Outline each blood parasite and name the species.
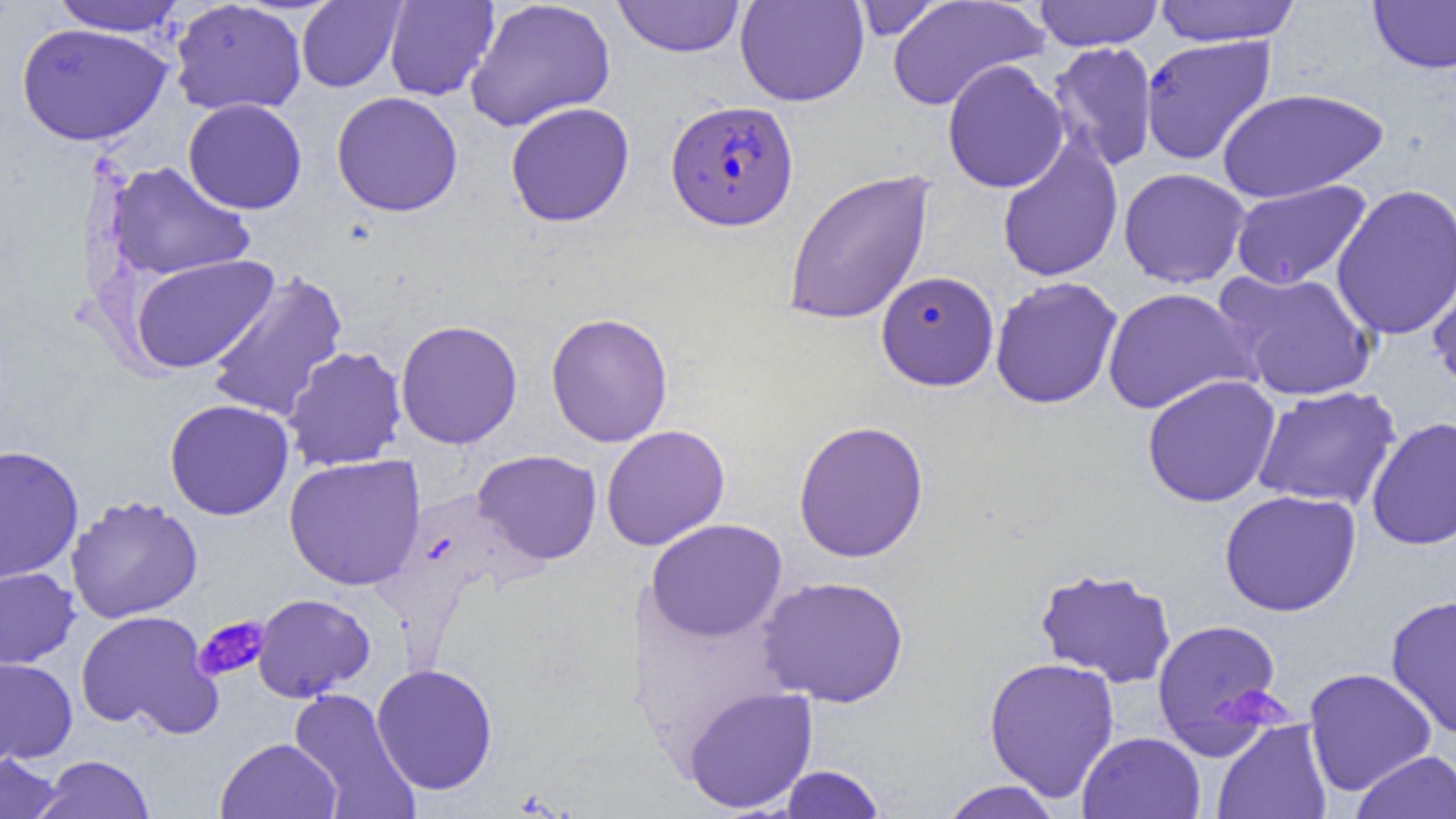

Approximate bounding boxes as named x1/y1/x2/y2 corners in pixels.
Plasmodium falciparum-infected red blood cells (subset): (x1=665, y1=99, x2=799, y2=231).
No Plasmodium ovale, Plasmodium malariae, Plasmodium vivax, Babesia divergens, or Trypanosoma brucei observed.

Summary:
  - Uninfected red blood cell locations (subset): (x1=384, y1=0, x2=499, y2=101), (x1=465, y1=0, x2=616, y2=132), (x1=612, y1=0, x2=746, y2=58), (x1=735, y1=0, x2=869, y2=107), (x1=848, y1=0, x2=947, y2=40), (x1=1032, y1=0, x2=1165, y2=51), (x1=1151, y1=0, x2=1302, y2=46), (x1=51, y1=1, x2=188, y2=37), (x1=169, y1=1, x2=307, y2=116), (x1=296, y1=1, x2=406, y2=92), (x1=887, y1=1, x2=1048, y2=112), (x1=1368, y1=1, x2=1456, y2=74), (x1=17, y1=23, x2=172, y2=146), (x1=1140, y1=35, x2=1278, y2=166), (x1=1046, y1=41, x2=1158, y2=172), (x1=942, y1=59, x2=1069, y2=193), (x1=1216, y1=87, x2=1389, y2=203), (x1=331, y1=91, x2=463, y2=217), (x1=183, y1=98, x2=307, y2=214), (x1=505, y1=101, x2=635, y2=227), (x1=996, y1=136, x2=1124, y2=283), (x1=105, y1=161, x2=254, y2=282), (x1=1118, y1=167, x2=1251, y2=289), (x1=783, y1=169, x2=935, y2=327), (x1=1230, y1=180, x2=1372, y2=290), (x1=1331, y1=184, x2=1456, y2=340), (x1=129, y1=254, x2=279, y2=373), (x1=1427, y1=257, x2=1456, y2=395), (x1=1215, y1=268, x2=1379, y2=402), (x1=205, y1=271, x2=348, y2=423), (x1=990, y1=276, x2=1123, y2=409), (x1=1102, y1=287, x2=1257, y2=415), (x1=545, y1=312, x2=674, y2=447), (x1=394, y1=319, x2=523, y2=450), (x1=282, y1=346, x2=408, y2=472), (x1=1142, y1=375, x2=1281, y2=508), (x1=1251, y1=385, x2=1401, y2=511), (x1=164, y1=399, x2=294, y2=520), (x1=1365, y1=416, x2=1456, y2=551), (x1=792, y1=419, x2=930, y2=563), (x1=601, y1=424, x2=730, y2=551), (x1=0, y1=445, x2=84, y2=584), (x1=472, y1=449, x2=602, y2=565), (x1=284, y1=454, x2=426, y2=591), (x1=1219, y1=490, x2=1362, y2=617), (x1=66, y1=495, x2=203, y2=624), (x1=645, y1=518, x2=787, y2=643), (x1=1034, y1=566, x2=1177, y2=688), (x1=0, y1=567, x2=80, y2=670), (x1=757, y1=575, x2=909, y2=707), (x1=252, y1=593, x2=376, y2=702), (x1=1385, y1=594, x2=1456, y2=738), (x1=75, y1=610, x2=221, y2=738), (x1=1151, y1=618, x2=1286, y2=756), (x1=0, y1=657, x2=78, y2=764), (x1=983, y1=657, x2=1120, y2=802), (x1=371, y1=663, x2=498, y2=795), (x1=1303, y1=667, x2=1437, y2=796), (x1=682, y1=685, x2=818, y2=814), (x1=288, y1=687, x2=420, y2=818), (x1=1211, y1=719, x2=1333, y2=819), (x1=1077, y1=732, x2=1207, y2=819), (x1=215, y1=737, x2=342, y2=819), (x1=0, y1=750, x2=66, y2=818), (x1=1349, y1=750, x2=1456, y2=819), (x1=33, y1=754, x2=156, y2=818), (x1=779, y1=764, x2=886, y2=818), (x1=938, y1=780, x2=1064, y2=819)
  - Platelet locations: (x1=194, y1=615, x2=270, y2=682)
  - Slide-level diagnosis: Plasmodium falciparum
  - Modality: light microscopy
  - Magnification: 1000x
  - Preparation: thin blood film
  - Image size: 1456×819 pixels
  - Field of view: one of a larger specimen